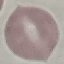 Result: negative for malaria parasites. Acquired by smartphone through the microscope eyepiece. Automatically extracted cell patch, resized to 64 × 64 pixels. Giemsa-stained preparation. Thin blood film.